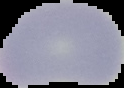

Image is 124×88 pixels. Segmented cell region on a black background. Result: no malaria parasites seen. From a thin blood smear.